Assess this cell for malaria.
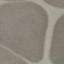
Uninfected.

Acquired by smartphone through the microscope eyepiece. Automatically extracted cell patch, resized to 64 × 64 pixels. Giemsa stain. Thin blood film.